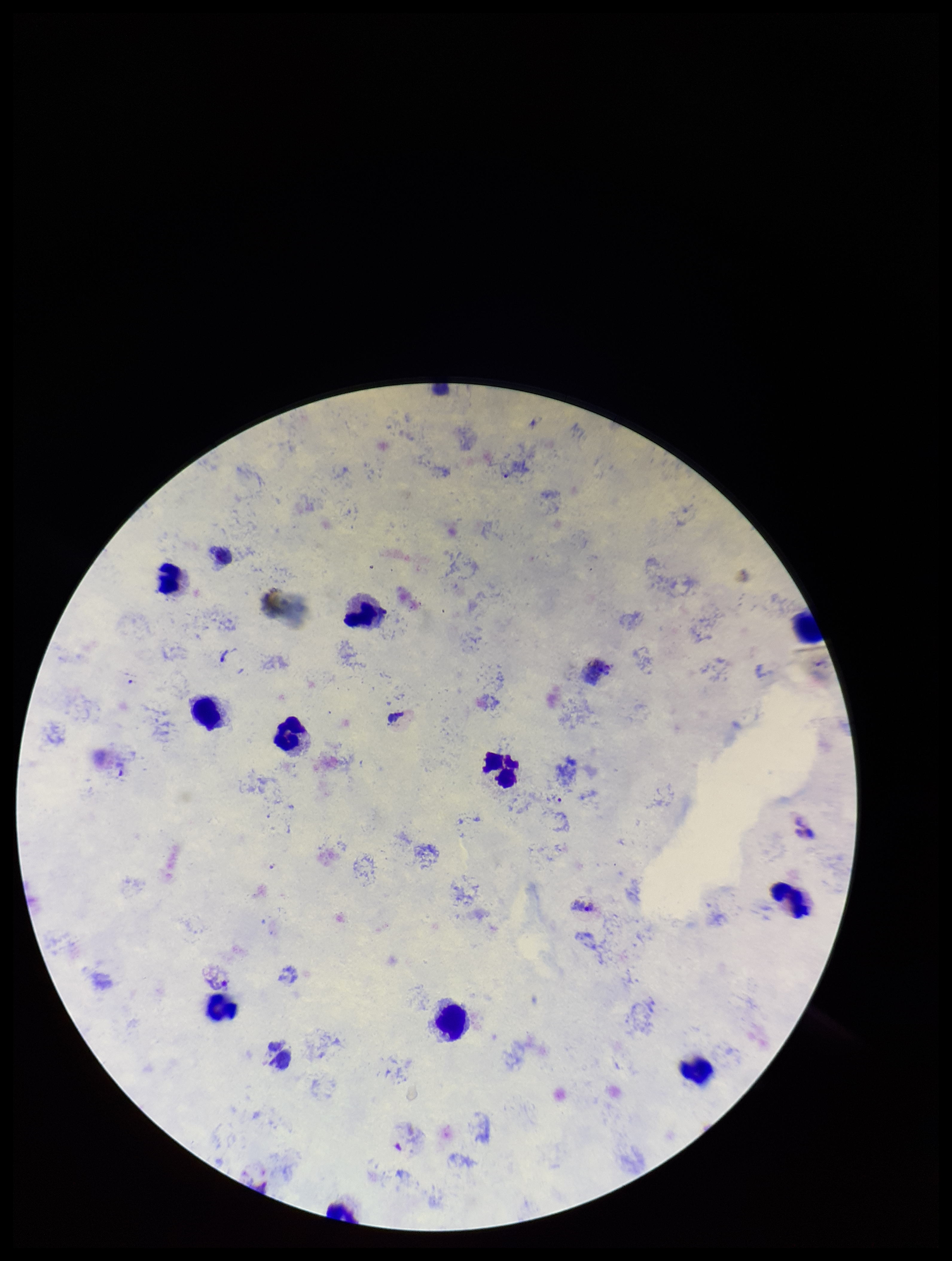
preparation = thick smear
parasite count = 3
patient malaria status = positive
stain = Giemsa
leukocyte count = 11
species reported for this patient = Plasmodium vivax
capture = smartphone photograph through the microscope eyepiece
Plasmodium parasites = detected
image size = 952×1261 pixels
field of view = one from this slide